Identify the parasite.
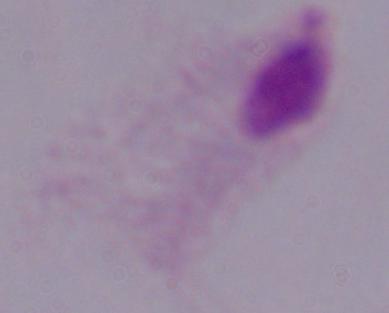
A trichomonad.

1000x magnification. Micrograph.